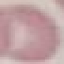
Malaria status: uninfected. Automatically extracted cell patch, resized to 64 × 64 pixels. Giemsa stain. Acquired by smartphone through the microscope eyepiece. Thin smear of blood.